Locate every malaria parasite and every leukocyte.
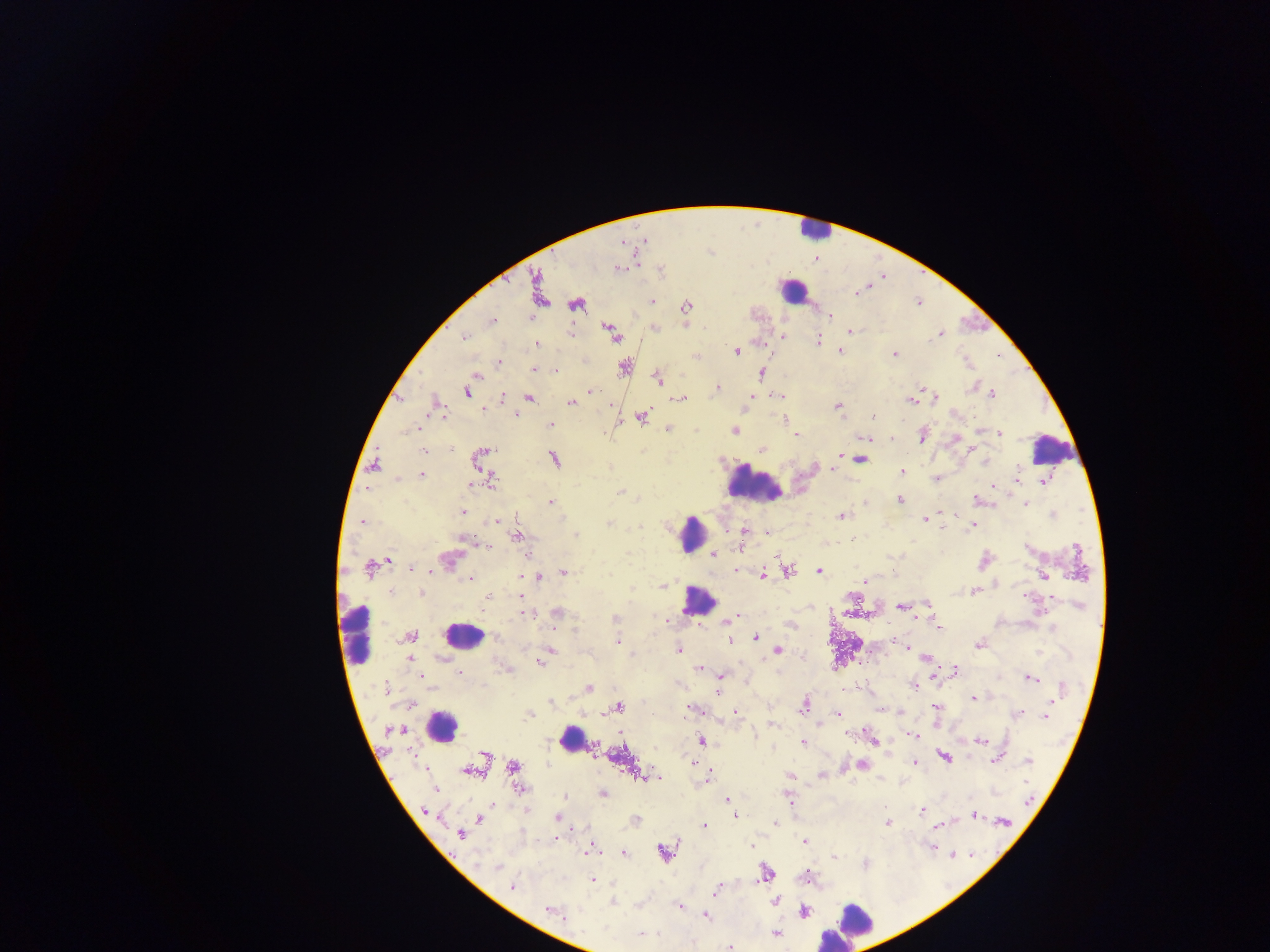
Approximate centers as {x, y} in pixels.
Malaria parasites: {645, 240}, {622, 241}, {815, 258}, {635, 264}, {618, 267}, {537, 284}, {854, 293}, {651, 301}, {918, 302}, {576, 303}, {686, 307}, {829, 314}, {529, 317}, {491, 320}, {687, 325}, {654, 327}, {849, 331}, {940, 333}, {570, 334}, {612, 334}, {782, 335}, {464, 336}, {818, 341}, {536, 344}, {763, 344}, {736, 351}, {839, 351}, {894, 354}, {695, 357}, {498, 363}, {624, 367}, {534, 370}, {554, 370}, {761, 373}, {474, 375}, {658, 379}, {972, 384}, {717, 387}, {466, 391}, {590, 391}, {990, 394}, {775, 396}, {398, 397}, {528, 397}, {501, 398}, {681, 398}, {747, 398}, {933, 398}, {911, 400}, {571, 402}, {436, 405}, {837, 406}, {481, 409}, {516, 414}, {641, 416}, {872, 416}, {785, 419}, {549, 425}, {668, 428}, {735, 430}, {978, 432}, {998, 433}, {796, 435}, {921, 435}, {865, 438}, {892, 438}, {955, 440}, {968, 446}, {974, 447}, {761, 448}, {423, 450}, {863, 453}, {478, 455}, {840, 455}, {836, 458}, {860, 458}, {553, 459}, {985, 462}, {374, 464}, {831, 470}, {901, 472}, {421, 474}, {396, 478}, {937, 478}, {490, 480}, {1015, 480}, {1044, 480}, {992, 487}, {621, 490}, {900, 499}, {978, 501}, {550, 502}, {1026, 503}, {462, 512}, {941, 512}, {1053, 513}, {840, 516}, {924, 518}, {496, 520}, {362, 521}, {609, 523}, {973, 525}, {747, 531}, {766, 532}, {574, 534}, {517, 537}, {463, 539}, {853, 541}, {741, 544}, {487, 545}, {712, 554}, {449, 559}, {984, 559}, {387, 560}, {368, 568}, {409, 568}, {734, 570}, {818, 570}, {788, 571}, {563, 572}, {538, 575}, {762, 575}, {1043, 576}, {520, 577}, {470, 578}, {865, 581}, {996, 584}, {662, 586}, {974, 591}, {422, 593}, {488, 597}, {519, 597}, {1051, 597}, {927, 603}, {1079, 605}, {901, 606}, {529, 612}, {556, 613}, {850, 613}, {615, 619}, {667, 621}, {729, 622}, {789, 624}, {939, 629}, {409, 636}, {496, 636}, {756, 637}, {892, 638}, {729, 640}, {616, 641}, {978, 644}, {907, 647}, {678, 649}, {551, 650}, {777, 651}, {804, 656}, {926, 657}, {410, 658}, {544, 658}, {540, 662}, {699, 668}, {508, 670}, {955, 671}, {459, 672}, {420, 676}, {719, 677}, {933, 678}, {1030, 678}, {915, 685}, {588, 688}, {386, 689}, {716, 693}, {972, 698}, {551, 701}, {410, 702}, {804, 703}, {618, 707}, {935, 707}, {694, 709}, {880, 709}, {735, 711}, {900, 711}, {1017, 713}, {529, 714}, {837, 714}, {1045, 717}, {771, 724}, {399, 730}, {622, 733}, {846, 734}, {915, 735}, {700, 740}, {978, 740}, {802, 741}, {873, 742}, {944, 757}, {996, 759}, {1028, 760}, {694, 763}, {916, 763}, {861, 765}, {512, 766}, {472, 769}, {821, 774}, {790, 775}, {645, 777}, {708, 777}, {519, 789}, {435, 790}, {603, 793}, {566, 796}, {727, 799}, {789, 801}, {492, 802}, {922, 810}, {426, 811}, {527, 811}, {735, 815}, {973, 815}, {557, 817}, {480, 819}, {635, 821}, {1003, 821}, {773, 823}, {886, 823}, {703, 825}, {937, 825}, {460, 834}, {805, 842}, {751, 846}, {932, 847}, {589, 848}, {663, 852}, {623, 853}, {952, 853}, {970, 854}, {833, 856}, {497, 867}, {766, 873}, {807, 876}, {592, 879}, {512, 887}, {715, 891}, {774, 901}, {613, 902}, {679, 906}, {549, 909}, {804, 911}, {705, 916}, {775, 933}, {730, 946}.
Leukocytes: {814, 230}, {792, 290}, {1053, 448}, {754, 484}, {690, 533}, {698, 600}, {357, 634}, {462, 637}, {439, 726}, {571, 738}, {848, 923}, {835, 937}.

Summary:
  - Image size: 1270×952 pixels
  - Capture: mobile-phone photograph through a microscope
  - Country: Ghana
  - Preparation: thick blood smear
  - Field of view: single